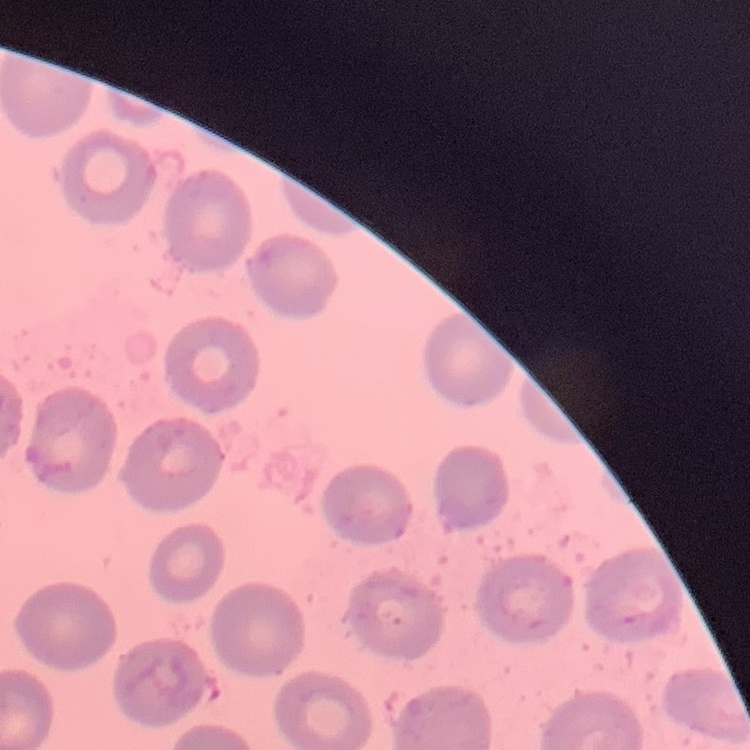

red_blood_cell_morphology: no rouleaux formation
image_type: square crop of a larger photomicrograph
preparation: thin blood smear
stain: Field's or Giemsa